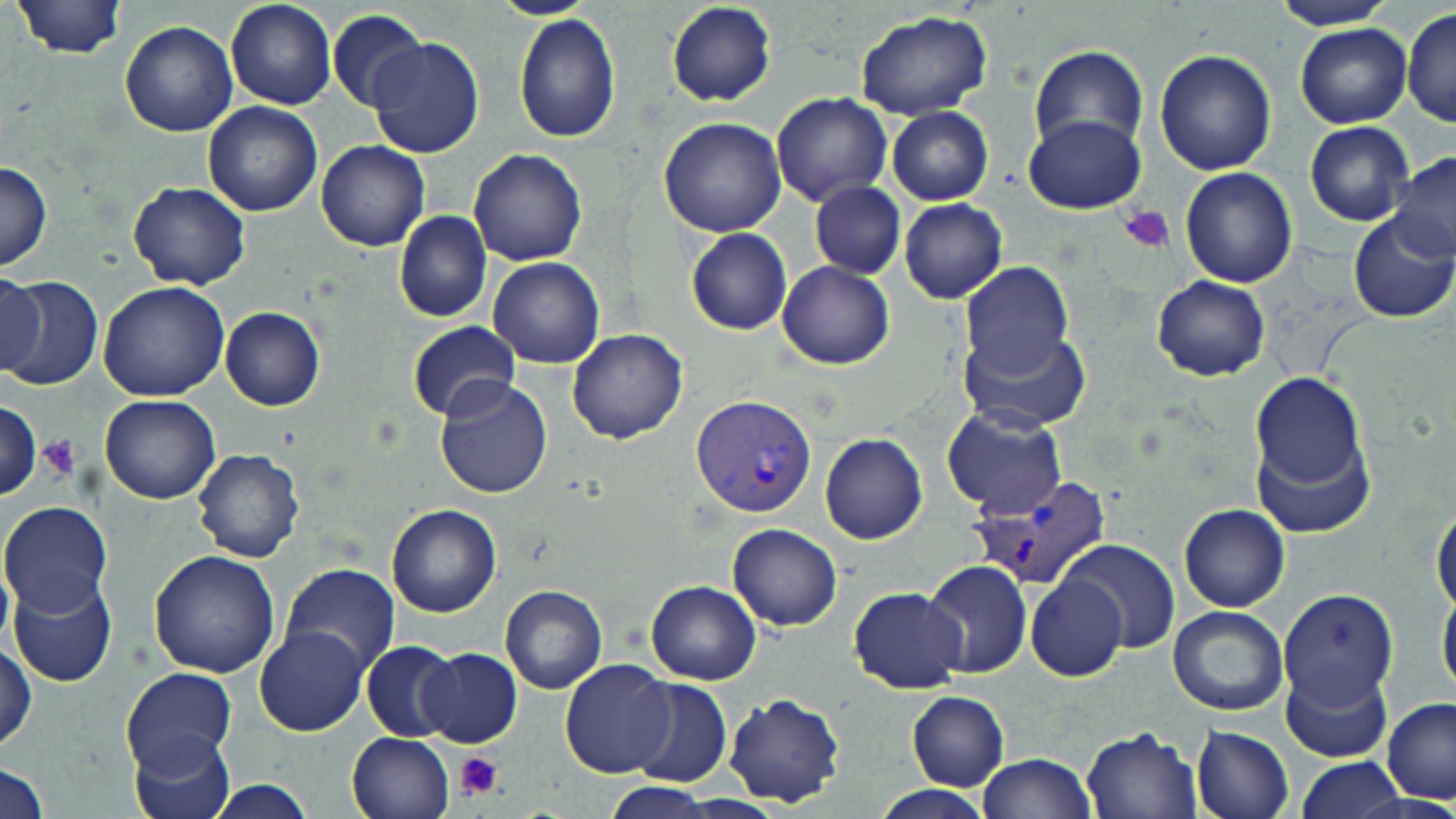
slide_level_diagnosis: Plasmodium vivax
image_size: 1456×819 pixels
platelet_locations: 'approximate bounding boxes as (x1, y1, x2, y2) in pixels: (1120, 202, 1176, 253), (39, 436, 78, 480), (455, 751, 503, 799)'
plasmodium_vivax_infected_red_blood_cell_locations: 'approximate bounding boxes as (x1, y1, x2, y2) in pixels: (693, 396, 817, 518), (972, 472, 1114, 592)'
modality: light microscopy
stain: May-Grünwald-Giemsa
magnification: 1000x
preparation: thin blood film
field_of_view: single
uninfected_red_blood_cell_locations: 'approximate bounding boxes as (x1, y1, x2, y2) in pixels: (225, 0, 337, 110), (492, 0, 595, 20), (666, 0, 777, 107), (1268, 0, 1398, 30), (15, 1, 125, 58), (327, 8, 428, 112), (1401, 9, 1456, 128), (854, 10, 992, 120), (513, 13, 621, 143), (118, 20, 238, 137), (1295, 22, 1411, 128), (366, 35, 485, 160), (1029, 44, 1147, 151), (1153, 50, 1277, 175), (771, 90, 893, 207), (203, 102, 323, 218), (887, 107, 994, 204), (1025, 114, 1147, 214), (658, 117, 788, 237), (1305, 121, 1414, 226), (316, 141, 430, 252), (468, 147, 588, 267), (1389, 151, 1456, 263), (0, 161, 51, 273), (1180, 167, 1299, 288), (127, 181, 252, 291), (810, 181, 906, 280), (899, 199, 1007, 303), (1348, 208, 1456, 322), (394, 211, 491, 324), (686, 228, 792, 336), (487, 258, 605, 368), (776, 261, 894, 369), (958, 261, 1075, 379), (0, 272, 45, 378), (0, 276, 103, 391), (1150, 276, 1269, 381), (98, 281, 231, 403), (220, 306, 325, 412), (406, 321, 520, 422), (961, 326, 1091, 431), (566, 329, 688, 444), (1247, 369, 1373, 526), (434, 373, 554, 497), (99, 394, 220, 505), (0, 399, 41, 501), (943, 409, 1067, 518), (167, 416, 291, 536), (820, 432, 927, 545), (192, 449, 305, 563), (1431, 498, 1456, 616), (1, 501, 112, 616), (1178, 503, 1290, 613), (387, 505, 500, 617), (727, 523, 842, 633), (1059, 540, 1180, 655), (148, 551, 281, 677), (922, 560, 1031, 678), (278, 564, 398, 676), (9, 573, 118, 687), (1026, 573, 1127, 682), (646, 580, 761, 685), (1438, 583, 1456, 703), (500, 585, 607, 694), (847, 588, 968, 694), (1277, 588, 1398, 709), (1167, 606, 1288, 715), (254, 627, 370, 738), (1, 640, 36, 752), (361, 642, 460, 739), (417, 648, 521, 748), (560, 658, 675, 779), (1279, 661, 1393, 763), (121, 667, 238, 773), (624, 676, 731, 786), (906, 691, 1010, 792), (723, 692, 846, 807), (1381, 697, 1456, 803), (1191, 724, 1294, 819), (1081, 727, 1202, 818), (130, 730, 232, 819), (347, 732, 454, 819), (978, 753, 1097, 818), (1295, 756, 1406, 819), (0, 760, 49, 819), (206, 778, 318, 819), (602, 780, 714, 817), (870, 785, 995, 819)'